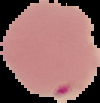
Image is 100×103 pixels. Malaria status: parasitized. Segmented cell region on a black background. From a thin blood film.